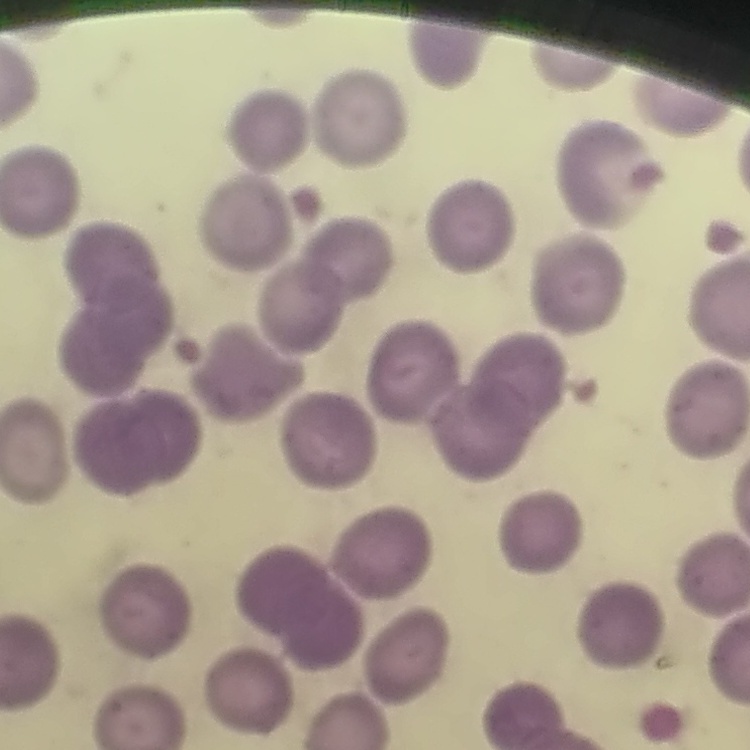

red blood cell morphology = no rouleaux formation
image type = one tile cut from a larger photomicrograph
stain = Field's or Giemsa
preparation = thin blood smear